Classify this cell by malaria status.
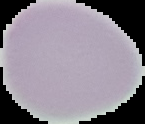
It is uninfected.

Cell region segmented out of the field of view; the surrounding area is masked to black. Image is 145×124 pixels. From a thin blood smear.